Identify the parasite.
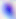
This is Toxoplasma gondii.

Summary:
  - Magnification: 400x
  - Modality: photomicrograph